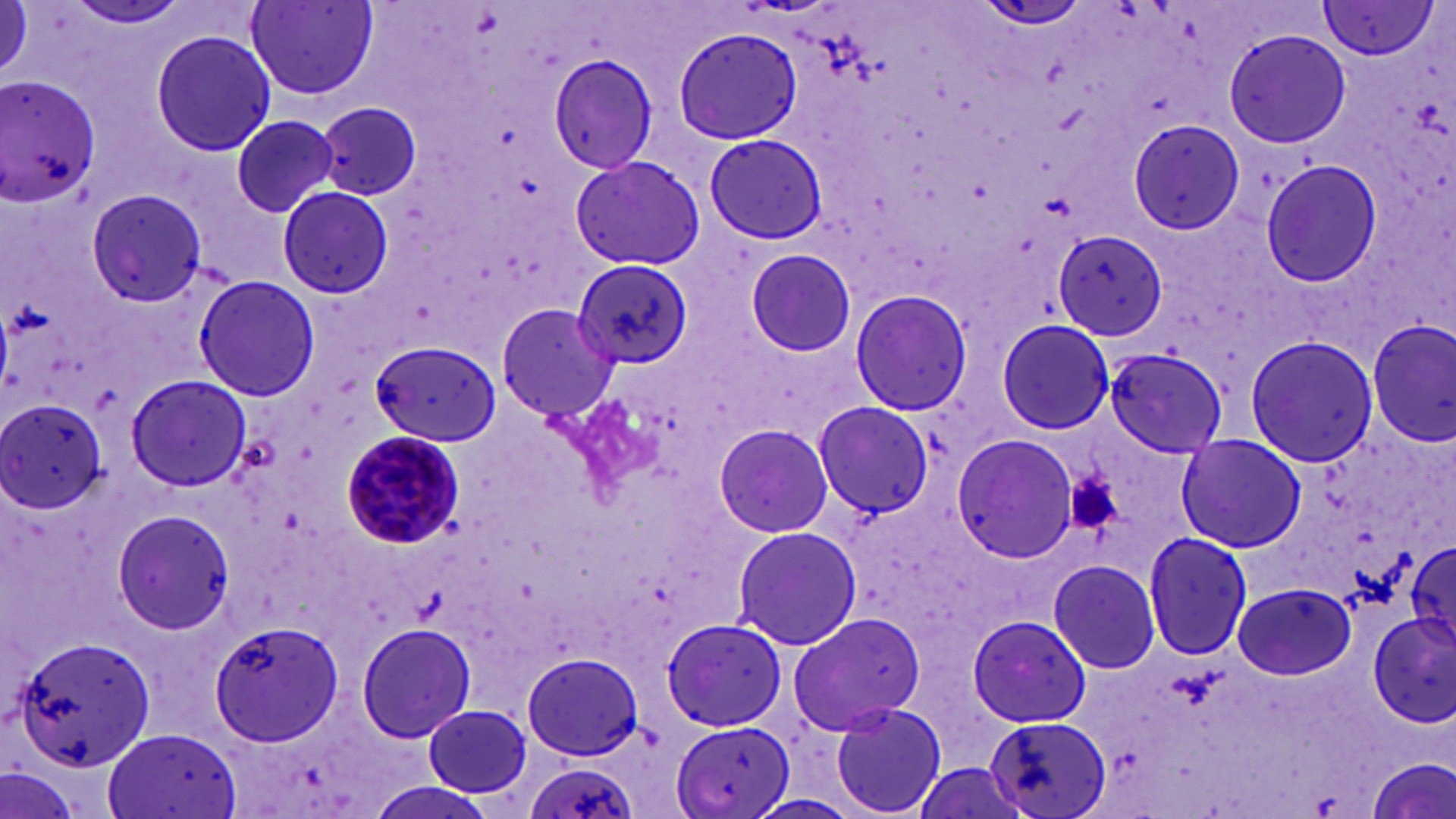
Summary:
  - Coordinate format: approximate bounding boxes as named x1/y1/x2/y2 corners in pixels
  - Plasmodium malariae-infected red blood cell locations: (x1=339, y1=430, x2=466, y2=550)
  - Platelet locations: (x1=1062, y1=467, x2=1130, y2=535)
  - Uninfected red blood cell locations: (x1=64, y1=0, x2=193, y2=32), (x1=246, y1=1, x2=377, y2=101), (x1=1313, y1=2, x2=1437, y2=62), (x1=0, y1=3, x2=32, y2=83), (x1=977, y1=3, x2=1088, y2=30), (x1=673, y1=27, x2=805, y2=145), (x1=1225, y1=29, x2=1351, y2=148), (x1=152, y1=30, x2=276, y2=157), (x1=546, y1=53, x2=658, y2=174), (x1=1, y1=76, x2=102, y2=208), (x1=315, y1=100, x2=424, y2=197), (x1=318, y1=102, x2=423, y2=199), (x1=230, y1=114, x2=341, y2=219), (x1=1124, y1=118, x2=1247, y2=237), (x1=704, y1=132, x2=827, y2=244), (x1=709, y1=132, x2=834, y2=241), (x1=571, y1=154, x2=704, y2=271), (x1=1263, y1=160, x2=1386, y2=284), (x1=278, y1=184, x2=394, y2=300), (x1=84, y1=188, x2=210, y2=308), (x1=1054, y1=232, x2=1165, y2=339), (x1=742, y1=248, x2=859, y2=357), (x1=572, y1=260, x2=692, y2=367), (x1=193, y1=276, x2=318, y2=402), (x1=849, y1=288, x2=974, y2=417), (x1=499, y1=306, x2=617, y2=423), (x1=1368, y1=318, x2=1455, y2=446), (x1=996, y1=319, x2=1115, y2=436), (x1=1365, y1=320, x2=1455, y2=449), (x1=1244, y1=335, x2=1380, y2=467), (x1=374, y1=344, x2=504, y2=444), (x1=1104, y1=346, x2=1225, y2=458), (x1=1101, y1=347, x2=1228, y2=458), (x1=126, y1=374, x2=251, y2=492), (x1=0, y1=396, x2=108, y2=514), (x1=810, y1=400, x2=931, y2=517), (x1=815, y1=404, x2=936, y2=516), (x1=712, y1=423, x2=833, y2=537), (x1=1175, y1=432, x2=1308, y2=554), (x1=949, y1=435, x2=1076, y2=559), (x1=111, y1=509, x2=232, y2=632), (x1=730, y1=526, x2=860, y2=649), (x1=1142, y1=531, x2=1252, y2=662), (x1=1405, y1=536, x2=1456, y2=661), (x1=1047, y1=558, x2=1162, y2=674), (x1=1231, y1=583, x2=1355, y2=679), (x1=786, y1=611, x2=928, y2=736), (x1=1365, y1=613, x2=1455, y2=729), (x1=967, y1=615, x2=1092, y2=728), (x1=659, y1=618, x2=785, y2=731), (x1=210, y1=621, x2=342, y2=745), (x1=357, y1=622, x2=477, y2=741), (x1=8, y1=632, x2=160, y2=774), (x1=523, y1=651, x2=646, y2=761), (x1=829, y1=702, x2=948, y2=817), (x1=425, y1=704, x2=532, y2=798), (x1=985, y1=717, x2=1111, y2=819), (x1=674, y1=719, x2=795, y2=819), (x1=100, y1=729, x2=239, y2=819), (x1=1364, y1=755, x2=1454, y2=819), (x1=523, y1=760, x2=637, y2=819), (x1=0, y1=765, x2=81, y2=819), (x1=366, y1=782, x2=491, y2=819)
  - Slide-level diagnosis: Plasmodium malariae
  - Modality: light microscopy
  - Stain: May-Grünwald-Giemsa
  - Preparation: thin blood film
  - Field of view: one of a larger specimen
  - Image size: 1456×819 pixels
  - Magnification: 1000x